Describe the morphology of the erythrocytes.
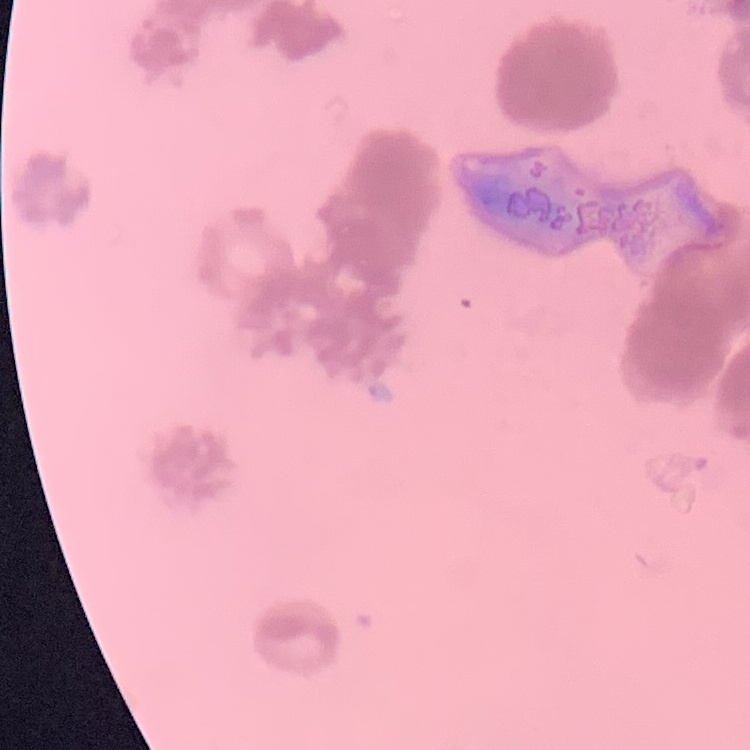
Rouleaux formation.

image_type: one tile cut from a larger photomicrograph
stain: Field's or Giemsa
preparation: thin peripheral smear